Locate every blood parasite and identify its species.
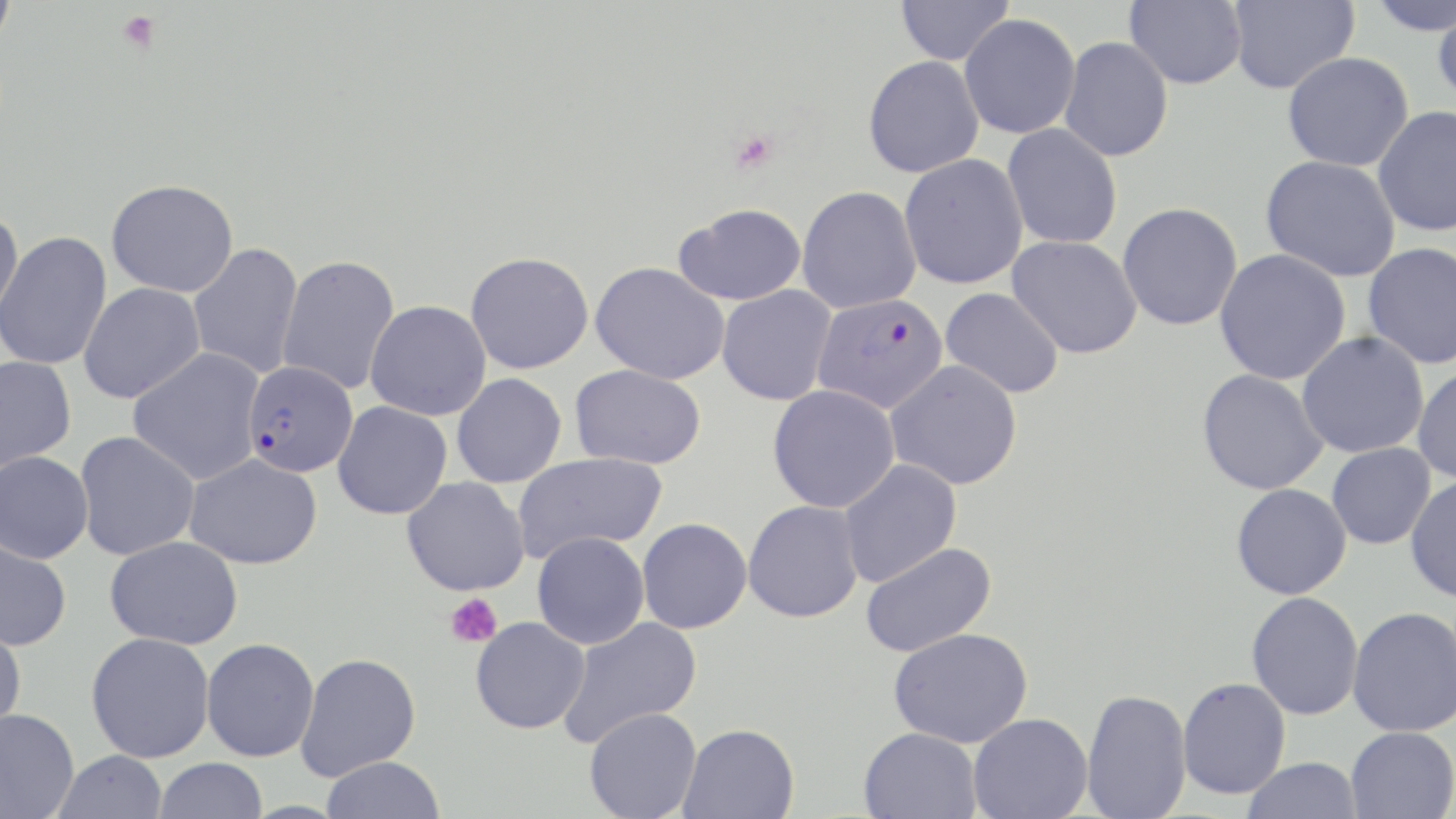

Approximate bounding boxes as (x1,y1)-(x2,y2) corner pairs in pixels.
Plasmodium falciparum-infected red blood cells: (813,292)-(949,413), (242,360)-(358,478).
No Plasmodium ovale, Plasmodium malariae, Plasmodium vivax, Babesia divergens, or Trypanosoma brucei observed.

Summary:
  - Platelet locations: (118,11)-(161,54), (728,129)-(778,173), (444,593)-(502,648)
  - Uninfected red blood cell locations: (0,0)-(18,53), (896,0)-(1014,65), (1124,0)-(1247,89), (1227,0)-(1359,94), (1364,1)-(1456,37), (1432,5)-(1456,107), (959,12)-(1081,140), (1059,36)-(1174,162), (1281,51)-(1415,172), (863,56)-(984,178), (1372,105)-(1456,237), (1002,123)-(1123,249), (899,153)-(1028,289), (1260,155)-(1401,282), (106,178)-(238,298), (797,185)-(922,313), (1117,202)-(1242,331), (674,203)-(807,306), (0,207)-(23,325), (0,231)-(113,370), (1007,235)-(1142,359), (187,242)-(304,380), (1362,242)-(1456,369), (1213,248)-(1351,385), (465,251)-(594,374), (277,255)-(401,395), (589,261)-(730,385), (78,282)-(205,404), (716,285)-(836,406), (940,287)-(1065,398), (365,300)-(491,420), (1296,332)-(1429,458), (128,348)-(265,485), (0,354)-(77,472), (884,359)-(1023,490), (570,363)-(706,469), (1412,365)-(1456,484), (1196,368)-(1329,495), (451,373)-(567,488), (767,385)-(900,513), (333,401)-(452,520), (75,431)-(200,560), (1326,442)-(1436,549), (0,450)-(94,564), (512,452)-(667,562), (184,453)-(323,569), (837,459)-(962,587), (1404,475)-(1456,603), (402,476)-(530,596), (1230,483)-(1351,600), (743,500)-(863,623), (636,517)-(752,634), (532,531)-(650,649), (105,535)-(244,649), (0,536)-(73,651), (859,541)-(997,658), (1247,591)-(1363,721), (1347,606)-(1456,737), (470,616)-(590,734), (556,616)-(702,749), (0,619)-(27,739), (888,627)-(1033,748), (86,632)-(215,763), (201,638)-(319,762), (295,653)-(421,781), (1177,677)-(1290,799), (1081,688)-(1192,818), (583,706)-(702,819), (0,708)-(79,819), (968,713)-(1093,819), (678,723)-(799,818), (1345,726)-(1456,819), (858,727)-(983,819), (53,750)-(169,819), (320,756)-(445,819), (153,757)-(269,818), (1242,757)-(1363,818)
  - Slide-level diagnosis: Plasmodium falciparum
  - Image size: 1456×819 pixels
  - Stain: May-Grünwald-Giemsa
  - Magnification: 1000x
  - Modality: optical microscopy
  - Preparation: thin blood smear
  - Field of view: one of a larger specimen